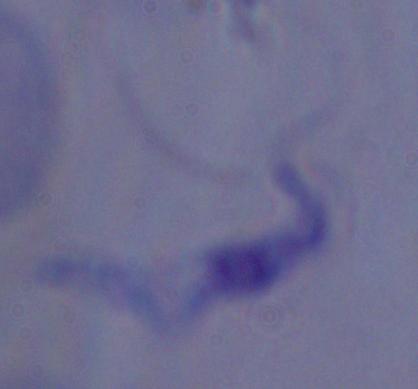
magnification = 1000x
modality = micrograph
identification = trypanosome